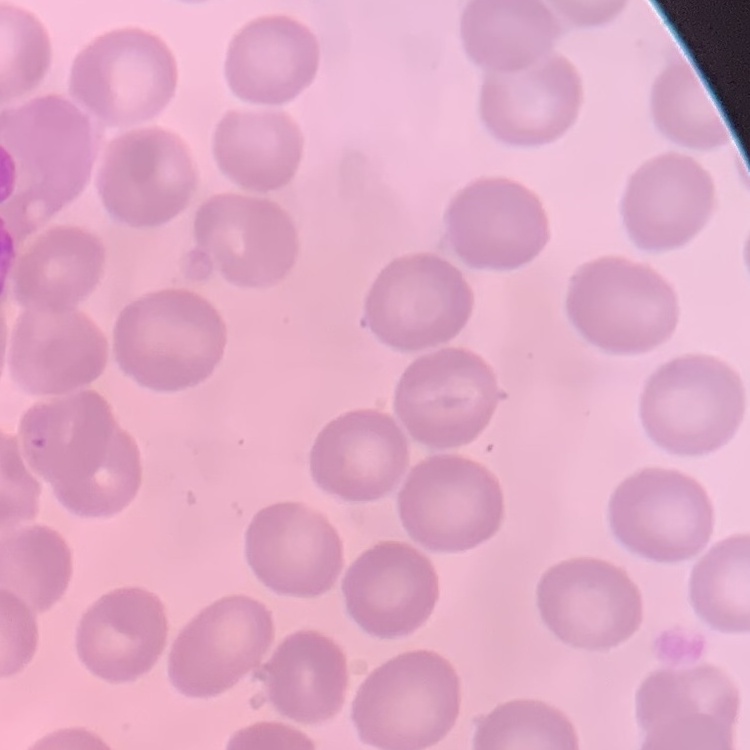 The erythrocytes show no rouleaux formation. One tile cut from a larger photomicrograph. Thin blood smear. Field's or Giemsa stain.